Name the parasite shown.
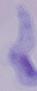
This is a trypanosome.

Photomicrograph. Captured at 1000x magnification.